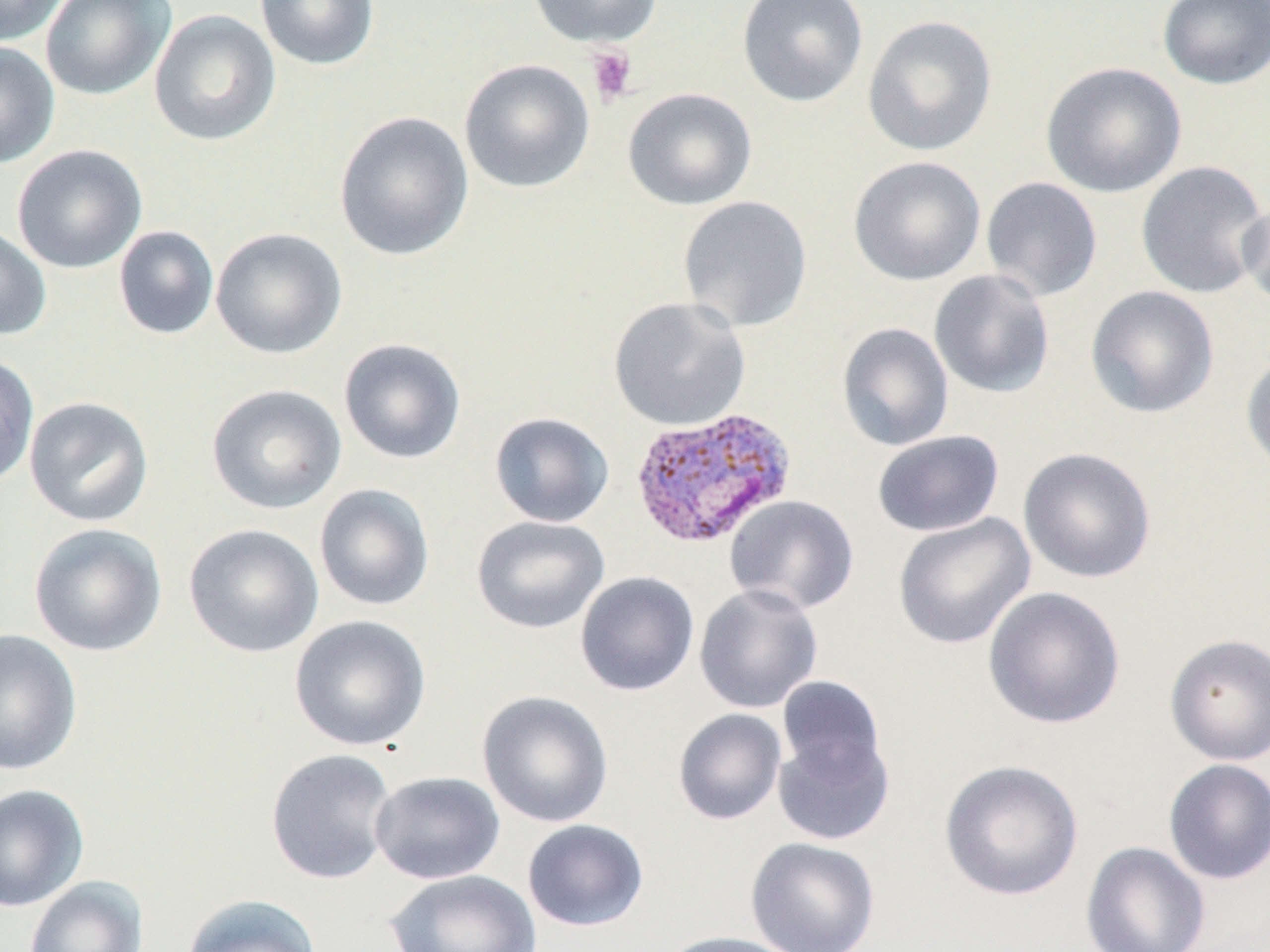
{
  "slide_level_diagnosis": "Plasmodium vivax",
  "preparation": "thin blood smear",
  "modality": "optical microscopy",
  "platelet_locations": "approximate bounding boxes as named x1/y1/x2/y2 corners in pixels: (x1=585, y1=45, x2=638, y2=106)",
  "image_size": "1270×952 pixels",
  "magnification": "1000x",
  "uninfected_red_blood_cell_locations": "approximate bounding boxes as named x1/y1/x2/y2 corners in pixels: (x1=0, y1=0, x2=67, y2=47), (x1=40, y1=0, x2=175, y2=101), (x1=255, y1=0, x2=380, y2=70), (x1=527, y1=0, x2=663, y2=48), (x1=736, y1=0, x2=869, y2=108), (x1=1157, y1=0, x2=1270, y2=90), (x1=149, y1=10, x2=281, y2=146), (x1=862, y1=15, x2=997, y2=156), (x1=0, y1=42, x2=60, y2=169), (x1=458, y1=59, x2=595, y2=193), (x1=1041, y1=61, x2=1188, y2=198), (x1=622, y1=87, x2=758, y2=210), (x1=334, y1=111, x2=474, y2=261), (x1=11, y1=144, x2=148, y2=274), (x1=848, y1=155, x2=986, y2=286), (x1=1135, y1=160, x2=1269, y2=299), (x1=980, y1=177, x2=1103, y2=302), (x1=677, y1=195, x2=813, y2=333), (x1=1238, y1=197, x2=1270, y2=310), (x1=0, y1=225, x2=52, y2=341), (x1=113, y1=225, x2=219, y2=339), (x1=210, y1=227, x2=348, y2=359), (x1=929, y1=269, x2=1055, y2=399), (x1=1085, y1=285, x2=1219, y2=419), (x1=608, y1=296, x2=751, y2=432), (x1=837, y1=322, x2=954, y2=451), (x1=338, y1=337, x2=467, y2=464), (x1=1240, y1=349, x2=1270, y2=477), (x1=0, y1=350, x2=39, y2=488), (x1=206, y1=383, x2=347, y2=514), (x1=24, y1=396, x2=154, y2=527), (x1=489, y1=412, x2=615, y2=528), (x1=872, y1=430, x2=1004, y2=538), (x1=1018, y1=447, x2=1157, y2=583), (x1=314, y1=484, x2=435, y2=611), (x1=724, y1=494, x2=859, y2=614), (x1=893, y1=512, x2=1036, y2=650), (x1=471, y1=515, x2=610, y2=634), (x1=29, y1=523, x2=167, y2=657), (x1=183, y1=523, x2=324, y2=658), (x1=575, y1=571, x2=700, y2=696), (x1=693, y1=583, x2=823, y2=714), (x1=982, y1=585, x2=1126, y2=730), (x1=289, y1=614, x2=432, y2=751), (x1=0, y1=628, x2=82, y2=776), (x1=1165, y1=633, x2=1270, y2=765), (x1=776, y1=676, x2=888, y2=786), (x1=477, y1=690, x2=613, y2=828), (x1=672, y1=708, x2=787, y2=825), (x1=772, y1=730, x2=893, y2=846), (x1=265, y1=748, x2=397, y2=885), (x1=1163, y1=758, x2=1270, y2=885), (x1=939, y1=759, x2=1084, y2=901), (x1=369, y1=771, x2=505, y2=884), (x1=0, y1=783, x2=89, y2=912), (x1=522, y1=819, x2=649, y2=932), (x1=746, y1=836, x2=880, y2=952), (x1=1081, y1=841, x2=1211, y2=952), (x1=385, y1=869, x2=543, y2=952), (x1=23, y1=876, x2=148, y2=952), (x1=181, y1=893, x2=323, y2=952), (x1=658, y1=931, x2=807, y2=952)",
  "field_of_view": "single",
  "stain": "May-Grünwald-Giemsa",
  "plasmodium_vivax_infected_red_blood_cell_locations": "approximate bounding boxes as named x1/y1/x2/y2 corners in pixels: (x1=629, y1=406, x2=797, y2=550)"
}